Assess this cell for malaria.
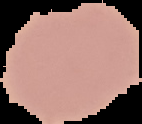

It is uninfected.

Summary:
  - Image type: cell region segmented out of the field of view; surrounding area masked to black
  - Preparation: thin blood film
  - Image size: 142×124 pixels